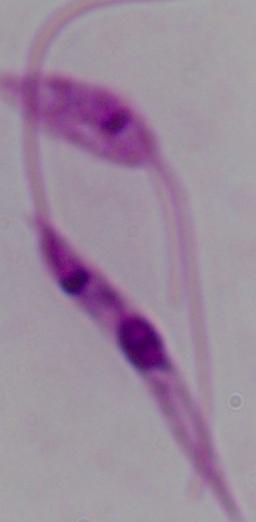
modality: micrograph
magnification: 1000x
identification: Leishmania